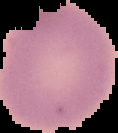
Summary:
  - Preparation: thin blood film
  - Result: no Plasmodium parasites detected
  - Image type: segmented cell region with the area outside set to black
  - Image size: 118×133 pixels